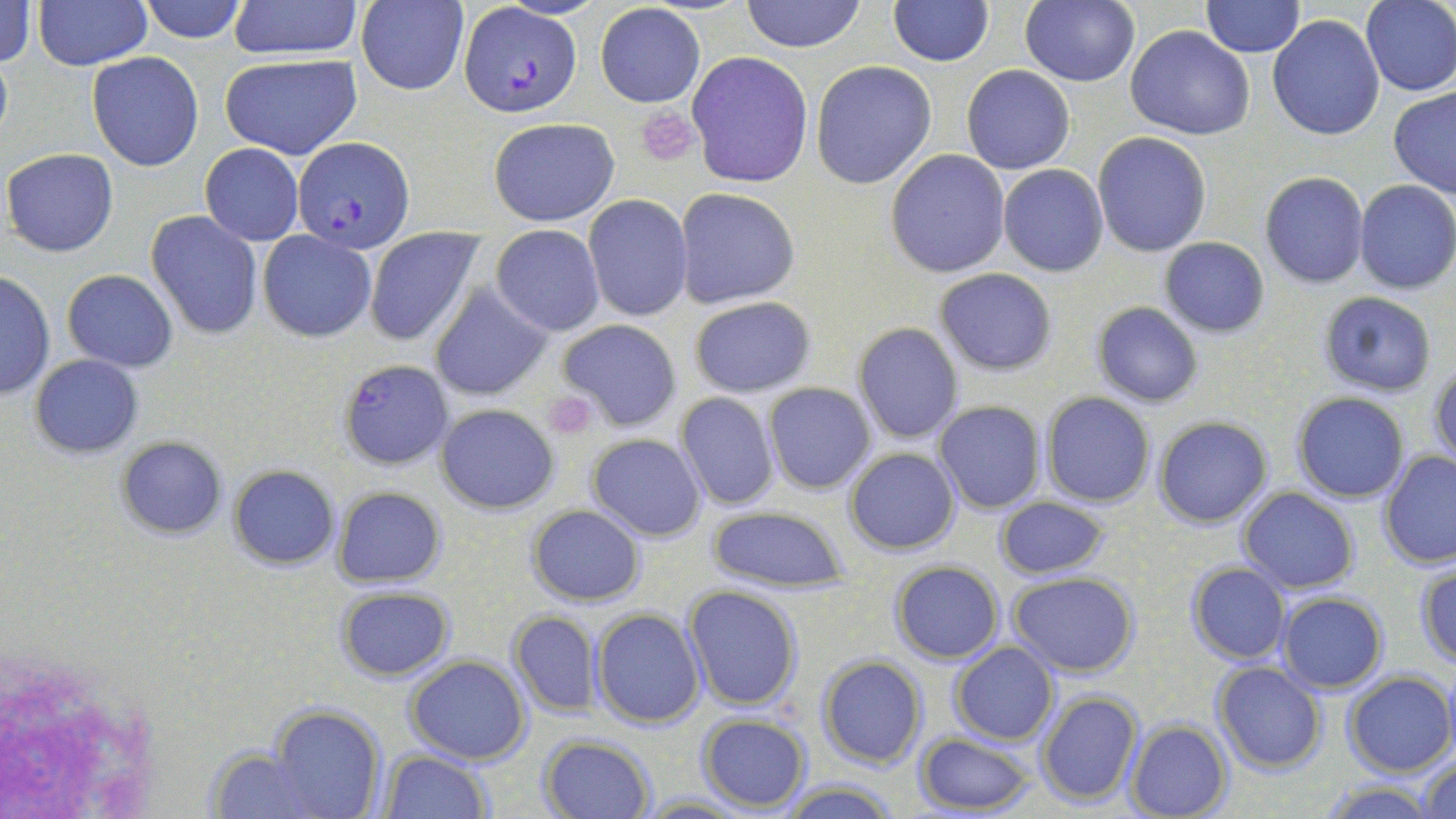

slide_level_diagnosis: Plasmodium falciparum
field_of_view: single
platelet_locations: 'approximate bounding boxes as [x1, y1, x2, y2] in pixels: [637, 107, 700, 166], [544, 389, 599, 439]'
plasmodium_falciparum_infected_red_blood_cell_locations: 'approximate bounding boxes as [x1, y1, x2, y2] in pixels: [458, 2, 582, 119], [293, 136, 417, 254], [338, 360, 453, 470]'
magnification: 1000x
modality: light microscopy
stain: May-Grünwald-Giemsa
uninfected_red_blood_cell_locations: 'approximate bounding boxes as [x1, y1, x2, y2] in pixels: [0, 0, 36, 68], [32, 0, 152, 70], [138, 0, 250, 44], [228, 0, 365, 58], [357, 0, 467, 95], [740, 0, 866, 51], [1022, 0, 1139, 86], [1201, 0, 1305, 56], [888, 1, 994, 67], [1360, 1, 1456, 96], [595, 4, 705, 108], [1266, 14, 1386, 141], [1125, 25, 1255, 142], [686, 51, 813, 188], [86, 52, 205, 172], [219, 53, 363, 161], [810, 60, 937, 190], [962, 64, 1075, 175], [1389, 88, 1456, 198], [488, 118, 620, 225], [1092, 132, 1212, 257], [200, 143, 304, 246], [2, 147, 120, 258], [885, 149, 1011, 278], [998, 166, 1108, 277], [1259, 172, 1369, 289], [1354, 179, 1456, 295], [674, 188, 800, 309], [583, 195, 694, 322], [146, 212, 263, 340], [492, 224, 605, 336], [363, 226, 483, 348], [259, 231, 377, 342], [1159, 237, 1271, 337], [934, 268, 1058, 376], [1, 269, 55, 399], [62, 269, 178, 372], [430, 284, 552, 400], [1317, 291, 1436, 397], [689, 296, 816, 397], [1091, 301, 1204, 409], [556, 319, 681, 433], [853, 322, 962, 443], [29, 354, 142, 458], [1429, 358, 1456, 469], [764, 384, 876, 495], [1291, 391, 1411, 503], [674, 392, 778, 510], [1041, 392, 1156, 508], [933, 400, 1046, 514], [435, 403, 559, 513], [1153, 415, 1273, 527], [586, 433, 707, 541], [115, 435, 227, 539], [844, 447, 961, 555], [1378, 450, 1456, 568], [228, 466, 339, 569], [333, 487, 446, 587], [1238, 487, 1359, 594], [996, 495, 1109, 580], [526, 504, 645, 607], [706, 506, 851, 594], [890, 561, 1003, 663], [1185, 562, 1291, 664], [1415, 562, 1456, 666], [1008, 571, 1139, 676], [682, 584, 805, 711], [334, 586, 457, 681], [1275, 592, 1389, 693], [592, 608, 706, 729], [508, 611, 603, 715], [949, 642, 1058, 745], [815, 655, 926, 769], [405, 656, 530, 764], [1211, 662, 1326, 773], [1342, 672, 1453, 777], [1035, 690, 1142, 807], [268, 707, 386, 819], [696, 714, 811, 810], [1123, 719, 1231, 819], [913, 733, 1038, 815], [540, 734, 656, 817], [201, 745, 324, 818], [380, 751, 492, 818], [1418, 757, 1456, 819], [778, 781, 902, 819], [1313, 782, 1441, 818], [639, 794, 752, 818]'
image_size: 1456×819 pixels
preparation: thin blood smear